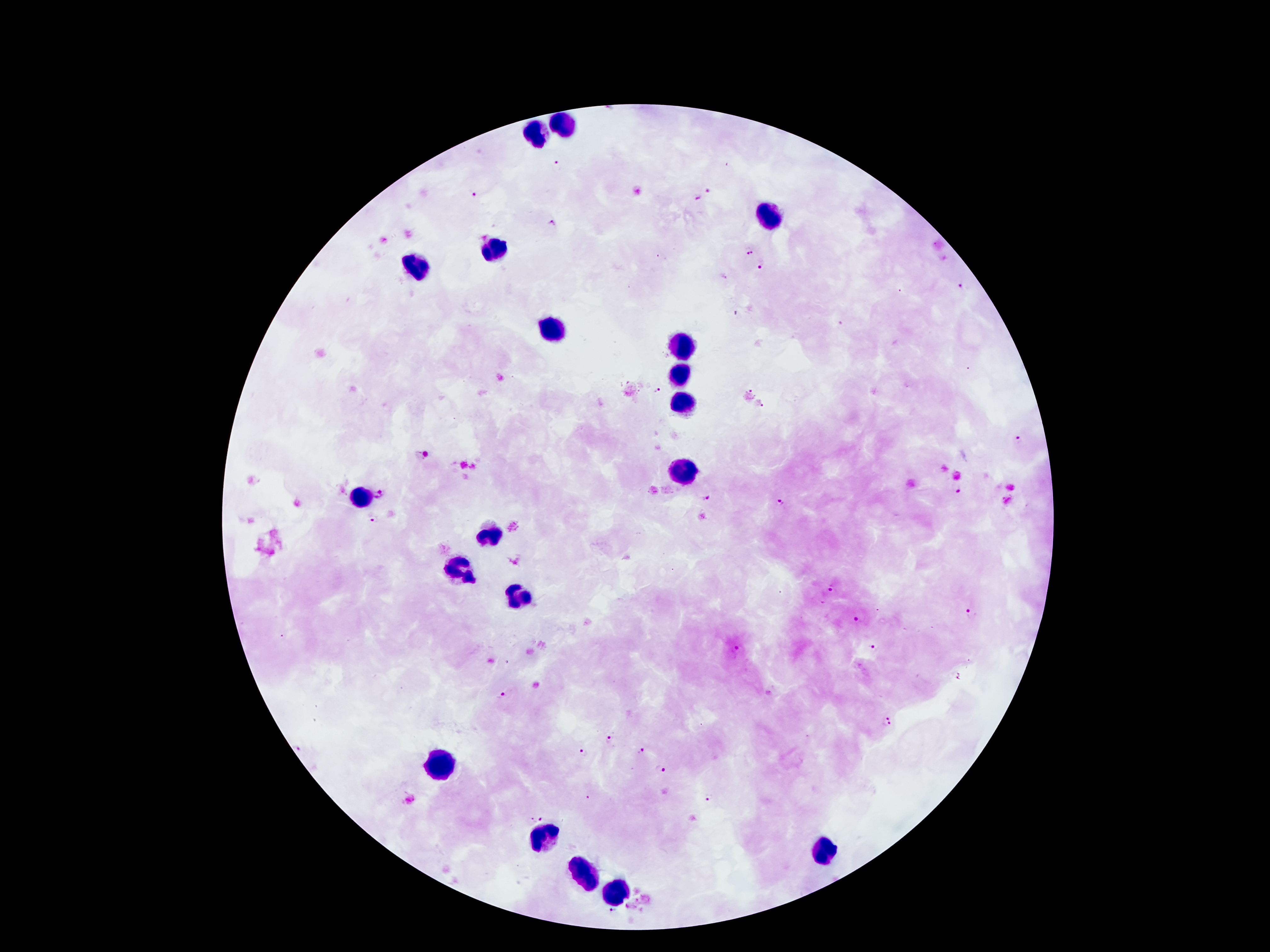
Approximate centers as {x, y} in pixels.
Summary:
  - Leukocyte locations: {564, 125}, {539, 134}, {768, 211}, {497, 247}, {419, 264}, {553, 329}, {684, 346}, {681, 377}, {681, 401}, {684, 468}, {360, 499}, {493, 537}, {461, 569}, {522, 592}, {440, 758}, {545, 839}, {828, 852}, {581, 873}, {616, 890}
  - Plasmodium parasite locations: {558, 163}, {709, 190}, {474, 194}, {697, 196}, {553, 223}, {749, 250}, {764, 267}, {963, 285}, {737, 313}, {655, 390}, {1019, 439}, {956, 488}, {382, 495}, {705, 498}, {783, 499}, {373, 520}, {831, 589}, {972, 613}, {856, 619}, {874, 645}, {738, 649}, {503, 694}, {888, 722}, {609, 739}, {580, 750}, {642, 751}, {660, 770}, {710, 798}, {537, 818}
  - Stain: Giemsa
  - Patient malaria status: positive for Plasmodium falciparum
  - Magnification: 100x
  - Image size: 1270×952 pixels
  - Preparation: thick peripheral-blood smear
  - Field of view: one from this slide
  - Capture: smartphone through the microscope eyepiece